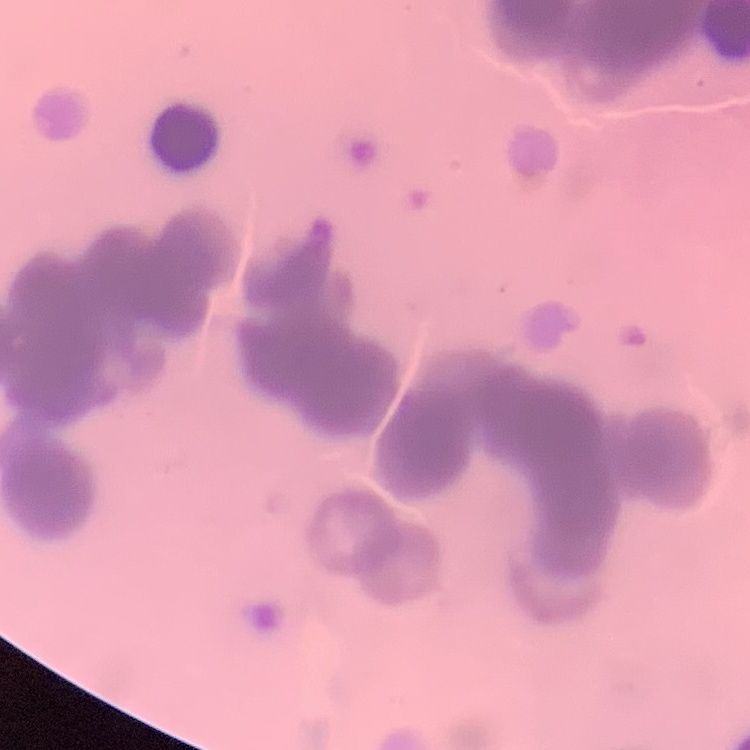

Summary:
  - Red blood cell morphology: rouleaux formation
  - Image type: one tile cut from a larger photomicrograph
  - Stain: Field's or Giemsa
  - Preparation: thin blood smear